Locate every Plasmodium parasite.
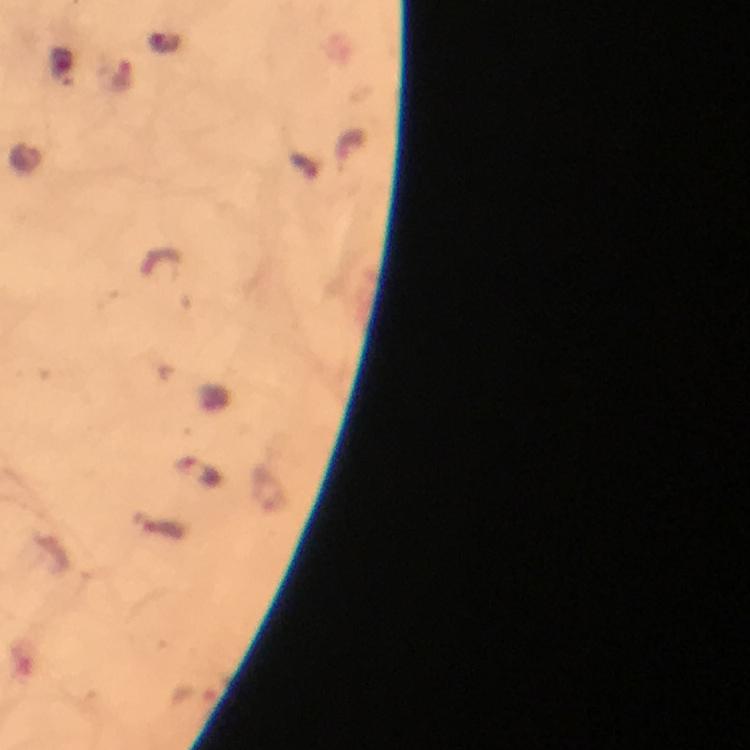
Approximate centers as {x, y} in pixels.
Plasmodium parasites: {121, 77}, {303, 167}, {199, 474}.

Summary:
  - Immersion oil: used
  - Cropped from: a single field of view
  - Context: from a diagnostic examination for malaria
  - Preparation: thick blood film
  - Magnification: 100x
  - Stain: Giemsa
  - Capture: smartphone mounted on the microscope
  - Image size: 750×750 pixels